Locate every Plasmodium parasite.
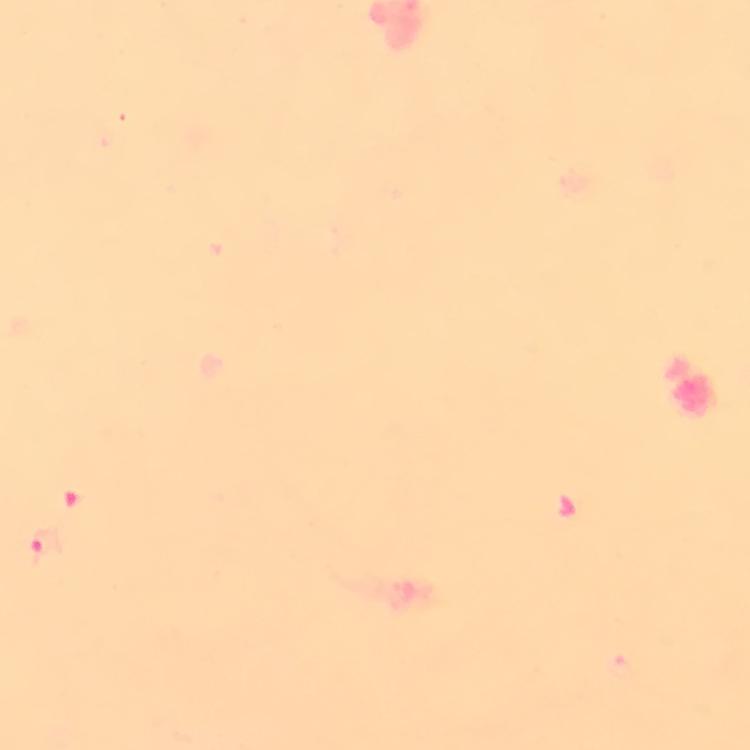

Approximate centers as {x, y} in pixels.
Plasmodium parasites: {43, 546}.

A crop from one field of view. Immersion oil was used. Thick blood film. Giemsa stain. Photographed through the microscope with a smartphone camera. From a diagnostic examination for malaria. At 100x magnification. Image is 750×750 pixels.